Locate and identify every blood parasite.
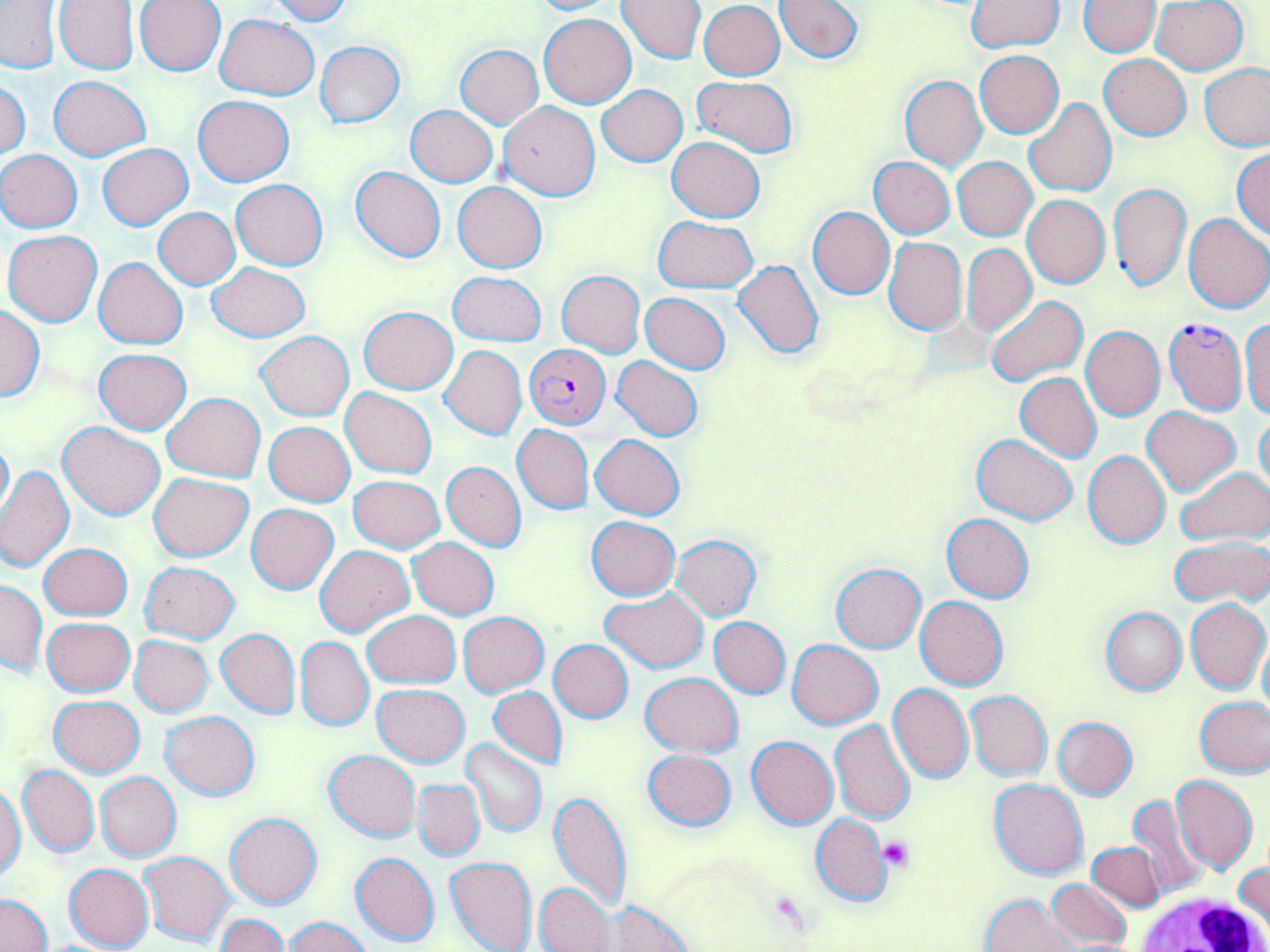
Approximate bounding boxes as (x1, y1, x2, y2) in pixels.
Plasmodium falciparum-infected red blood cells: (1163, 317, 1248, 417), (526, 344, 610, 427).
No Plasmodium ovale, Plasmodium malariae, Plasmodium vivax, Babesia divergens, or Trypanosoma brucei observed.

Summary:
  - White blood cell locations: (1134, 889, 1267, 952)
  - Platelet locations: (879, 836, 913, 871)
  - Uninfected red blood cell locations: (135, 0, 225, 75), (266, 0, 353, 25), (527, 0, 617, 15), (615, 0, 706, 65), (773, 0, 863, 63), (0, 1, 62, 73), (54, 1, 140, 74), (1079, 1, 1159, 55), (1151, 1, 1248, 74), (699, 2, 785, 80), (965, 2, 1063, 52), (538, 13, 636, 108), (214, 14, 318, 100), (314, 41, 405, 127), (454, 44, 543, 128), (975, 50, 1064, 136), (1098, 54, 1191, 141), (1201, 63, 1270, 151), (49, 76, 150, 160), (693, 76, 796, 158), (899, 76, 986, 171), (1, 79, 31, 161), (598, 85, 687, 166), (193, 95, 294, 186), (1024, 98, 1116, 198), (497, 101, 599, 199), (406, 106, 498, 186), (667, 136, 764, 221), (98, 144, 193, 230), (1232, 149, 1270, 240), (0, 150, 83, 232), (868, 156, 954, 239), (952, 156, 1036, 240), (350, 166, 446, 263), (231, 178, 329, 271), (453, 181, 547, 273), (1108, 182, 1191, 292), (1022, 195, 1109, 288), (807, 207, 894, 299), (154, 208, 239, 289), (1183, 213, 1270, 313), (652, 215, 757, 293), (3, 230, 102, 327), (883, 237, 967, 335), (961, 242, 1036, 337), (95, 258, 188, 349), (733, 260, 824, 359), (207, 263, 310, 341), (448, 271, 547, 346), (555, 271, 645, 358), (640, 292, 731, 374), (986, 295, 1088, 388), (358, 305, 459, 394), (0, 306, 44, 401), (1240, 319, 1270, 418), (1081, 326, 1164, 421), (256, 331, 354, 420), (439, 345, 527, 440), (94, 348, 192, 434), (612, 356, 704, 442), (1014, 372, 1101, 463), (341, 388, 436, 479), (163, 393, 266, 482), (1141, 405, 1240, 495), (1255, 415, 1270, 497), (264, 421, 355, 507), (58, 422, 165, 520), (512, 424, 593, 515), (0, 434, 14, 521), (973, 434, 1077, 525), (590, 435, 684, 520), (1083, 450, 1171, 548), (441, 462, 526, 551), (1, 466, 74, 572), (1177, 468, 1270, 545), (148, 472, 253, 561), (348, 475, 445, 552), (247, 503, 337, 595), (941, 514, 1033, 602), (586, 517, 680, 600), (672, 534, 762, 620), (1171, 536, 1270, 608), (409, 537, 499, 619), (40, 544, 131, 621), (314, 544, 414, 637), (141, 562, 240, 642), (830, 563, 925, 651), (1, 579, 47, 675), (600, 587, 708, 673), (914, 595, 1007, 689), (1184, 599, 1269, 694), (1101, 607, 1187, 693), (363, 610, 459, 688), (458, 611, 548, 695), (708, 616, 791, 698), (42, 617, 134, 696), (216, 628, 300, 718), (129, 636, 215, 716), (296, 636, 373, 731), (1259, 636, 1270, 725), (549, 639, 633, 722), (788, 640, 882, 728), (640, 672, 743, 756), (373, 684, 468, 766), (888, 684, 974, 784), (488, 688, 566, 768), (966, 691, 1051, 781), (838, 693, 964, 804), (49, 695, 145, 776), (1195, 696, 1270, 777), (160, 711, 260, 800), (1053, 716, 1137, 799), (830, 721, 916, 824), (747, 735, 838, 829), (460, 739, 546, 837), (642, 748, 736, 831), (324, 751, 421, 841), (18, 766, 98, 857), (96, 772, 181, 860), (1171, 773, 1257, 874), (413, 779, 484, 860), (990, 779, 1088, 880), (0, 784, 26, 883), (547, 789, 632, 910), (1123, 794, 1210, 899), (226, 813, 321, 909), (811, 813, 891, 907), (1086, 841, 1166, 911), (138, 851, 236, 947), (350, 852, 439, 947), (445, 855, 537, 952), (64, 863, 154, 950), (1234, 864, 1269, 938), (1045, 880, 1132, 948), (535, 882, 616, 952), (1, 893, 52, 952), (982, 894, 1082, 952), (609, 901, 694, 951), (216, 915, 290, 952), (283, 917, 372, 952)
  - Slide-level diagnosis: Plasmodium falciparum
  - Modality: optical microscopy
  - Stain: May-Grünwald-Giemsa
  - Field of view: one of a larger specimen
  - Image size: 1270×952 pixels
  - Magnification: 1000x
  - Preparation: thin blood smear